Classify this cell by malaria status.
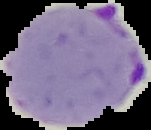

Parasitized.

image type = segmented cell region with the area outside set to black
preparation = thin blood smear
image size = 151×130 pixels